Locate and identify every blood parasite.
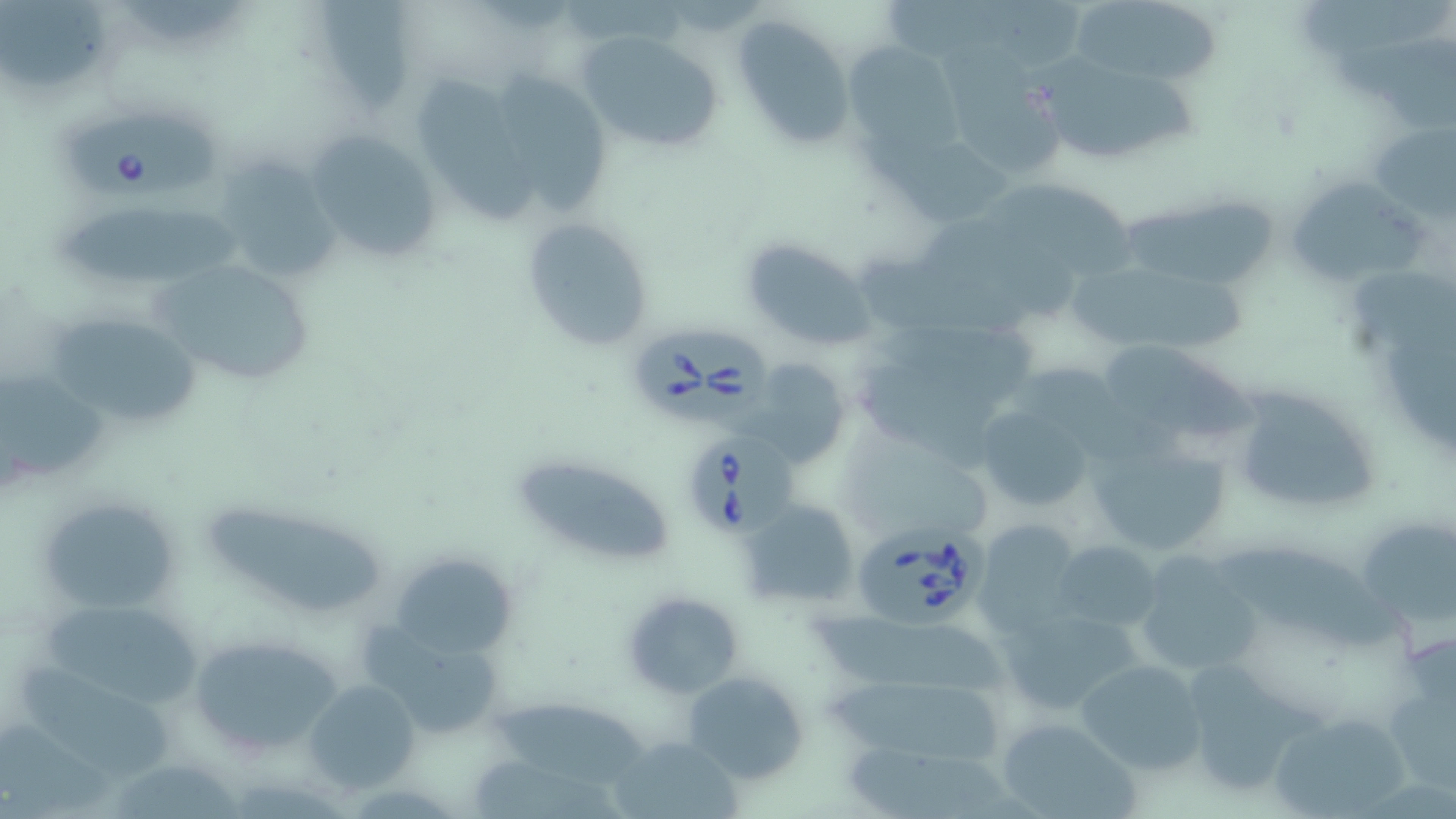

Approximate bounding boxes as named x1/y1/x2/y2 corners in pixels.
Babesia divergens-infected red blood cells: (x1=69, y1=110, x2=221, y2=196), (x1=632, y1=325, x2=772, y2=428), (x1=690, y1=432, x2=805, y2=537), (x1=856, y1=514, x2=987, y2=631).
No Plasmodium falciparum, Plasmodium ovale, Plasmodium malariae, Plasmodium vivax, or Trypanosoma brucei observed.

Summary:
  - Uninfected red blood cell locations: (x1=1299, y1=1, x2=1453, y2=60), (x1=1, y1=2, x2=114, y2=90), (x1=1074, y1=2, x2=1229, y2=87), (x1=318, y1=4, x2=408, y2=105), (x1=731, y1=14, x2=857, y2=152), (x1=575, y1=29, x2=725, y2=153), (x1=842, y1=41, x2=960, y2=152), (x1=945, y1=44, x2=1064, y2=177), (x1=1023, y1=52, x2=1200, y2=155), (x1=504, y1=71, x2=614, y2=210), (x1=420, y1=82, x2=544, y2=221), (x1=1370, y1=122, x2=1454, y2=216), (x1=303, y1=128, x2=442, y2=266), (x1=851, y1=131, x2=1018, y2=224), (x1=212, y1=158, x2=344, y2=284), (x1=985, y1=179, x2=1136, y2=279), (x1=1288, y1=182, x2=1430, y2=286), (x1=1118, y1=193, x2=1278, y2=286), (x1=56, y1=210, x2=244, y2=286), (x1=520, y1=216, x2=655, y2=351), (x1=741, y1=238, x2=877, y2=348), (x1=853, y1=251, x2=1029, y2=347), (x1=146, y1=255, x2=319, y2=389), (x1=1072, y1=264, x2=1252, y2=354), (x1=1353, y1=272, x2=1456, y2=361), (x1=44, y1=312, x2=204, y2=435), (x1=1109, y1=348, x2=1260, y2=444), (x1=749, y1=360, x2=848, y2=466), (x1=1022, y1=361, x2=1173, y2=465), (x1=0, y1=369, x2=111, y2=480), (x1=1227, y1=381, x2=1382, y2=516), (x1=975, y1=405, x2=1095, y2=511), (x1=1083, y1=436, x2=1230, y2=560), (x1=512, y1=453, x2=674, y2=565), (x1=38, y1=494, x2=183, y2=615), (x1=196, y1=495, x2=383, y2=614), (x1=739, y1=498, x2=859, y2=609), (x1=1355, y1=513, x2=1456, y2=631), (x1=973, y1=519, x2=1083, y2=635), (x1=1049, y1=539, x2=1163, y2=634), (x1=1216, y1=545, x2=1405, y2=653), (x1=391, y1=550, x2=518, y2=658), (x1=1131, y1=556, x2=1260, y2=678), (x1=621, y1=590, x2=743, y2=699), (x1=38, y1=597, x2=203, y2=708), (x1=996, y1=603, x2=1146, y2=713), (x1=359, y1=615, x2=508, y2=739), (x1=187, y1=634, x2=345, y2=756), (x1=1077, y1=658, x2=1205, y2=774), (x1=20, y1=661, x2=185, y2=780), (x1=1180, y1=662, x2=1319, y2=798), (x1=1382, y1=663, x2=1456, y2=793), (x1=686, y1=672, x2=809, y2=782), (x1=304, y1=679, x2=420, y2=793), (x1=496, y1=704, x2=652, y2=786), (x1=1267, y1=711, x2=1411, y2=819), (x1=994, y1=716, x2=1138, y2=818), (x1=3, y1=721, x2=118, y2=816), (x1=613, y1=733, x2=743, y2=819), (x1=469, y1=755, x2=625, y2=819)
  - Slide-level diagnosis: Babesia divergens
  - Field of view: single
  - Modality: light microscopy
  - Preparation: thin blood smear
  - Image size: 1456×819 pixels
  - Magnification: 1000x
  - Stain: May-Grünwald-Giemsa